Locate every blood parasite and identify its species.
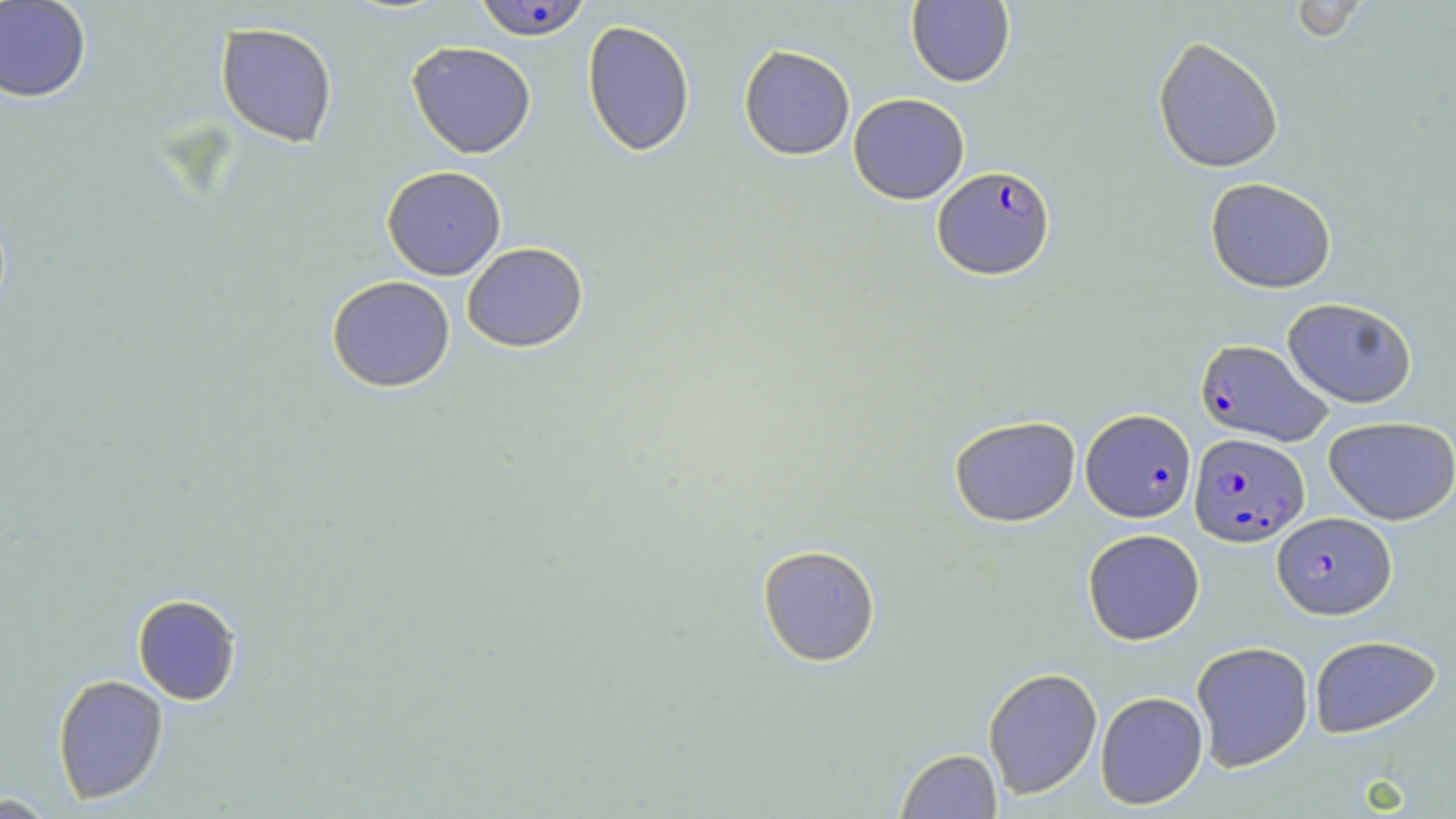
Approximate bounding boxes as [x1, y1, x2, y2] in pixels.
Plasmodium falciparum-infected red blood cells: [472, 0, 593, 42], [932, 165, 1055, 280], [1195, 339, 1333, 446], [1081, 408, 1196, 522], [1189, 432, 1310, 546], [1272, 512, 1397, 619].
No Plasmodium ovale, Plasmodium malariae, Plasmodium vivax, Babesia divergens, or Trypanosoma brucei observed.

Uninfected red blood cell locations: [0, 0, 92, 103], [1287, 0, 1371, 43], [906, 1, 1015, 87], [582, 20, 695, 157], [215, 22, 338, 148], [1152, 36, 1285, 173], [406, 41, 537, 158], [401, 43, 523, 281], [739, 44, 855, 160], [848, 93, 969, 204], [381, 165, 507, 280], [1205, 176, 1337, 293], [461, 242, 588, 352], [326, 275, 455, 393], [1282, 297, 1417, 408], [949, 415, 1081, 527], [1324, 416, 1456, 524], [1082, 528, 1205, 645], [757, 544, 881, 667], [132, 594, 242, 705], [1309, 634, 1442, 738], [1191, 641, 1314, 772], [983, 667, 1103, 799], [52, 674, 169, 804], [1095, 691, 1208, 810], [895, 748, 1002, 818], [1, 791, 64, 818]. Slide-level diagnosis: Plasmodium falciparum. May-Grünwald-Giemsa stain. Single field of view. Light microscopy. Captured at 1000x magnification. Image is 1456×819 pixels. Thin blood film.